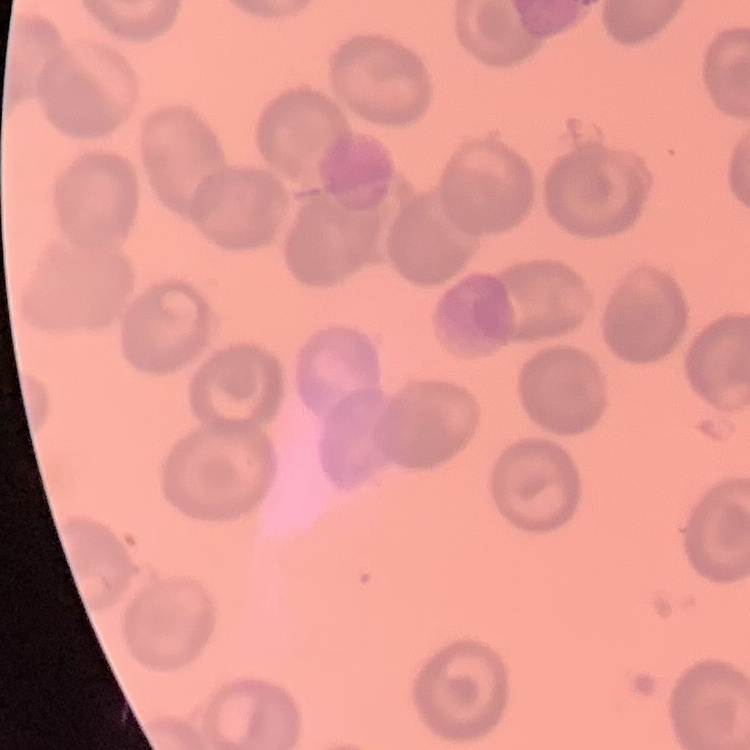
The erythrocytes show no rouleaux formation. Field's or Giemsa stain. Square crop of a larger photomicrograph. Thin blood film.